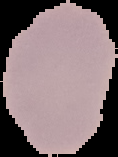

Summary:
  - Image size: 118×157 pixels
  - Malaria status: uninfected
  - Preparation: thin blood smear
  - Image type: segmented cell region on a black background